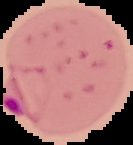

image type = cell region segmented out of the field of view; surrounding area masked to black
image size = 133×145 pixels
result = malaria parasites identified
preparation = thin blood smear